State the blood parasite species.
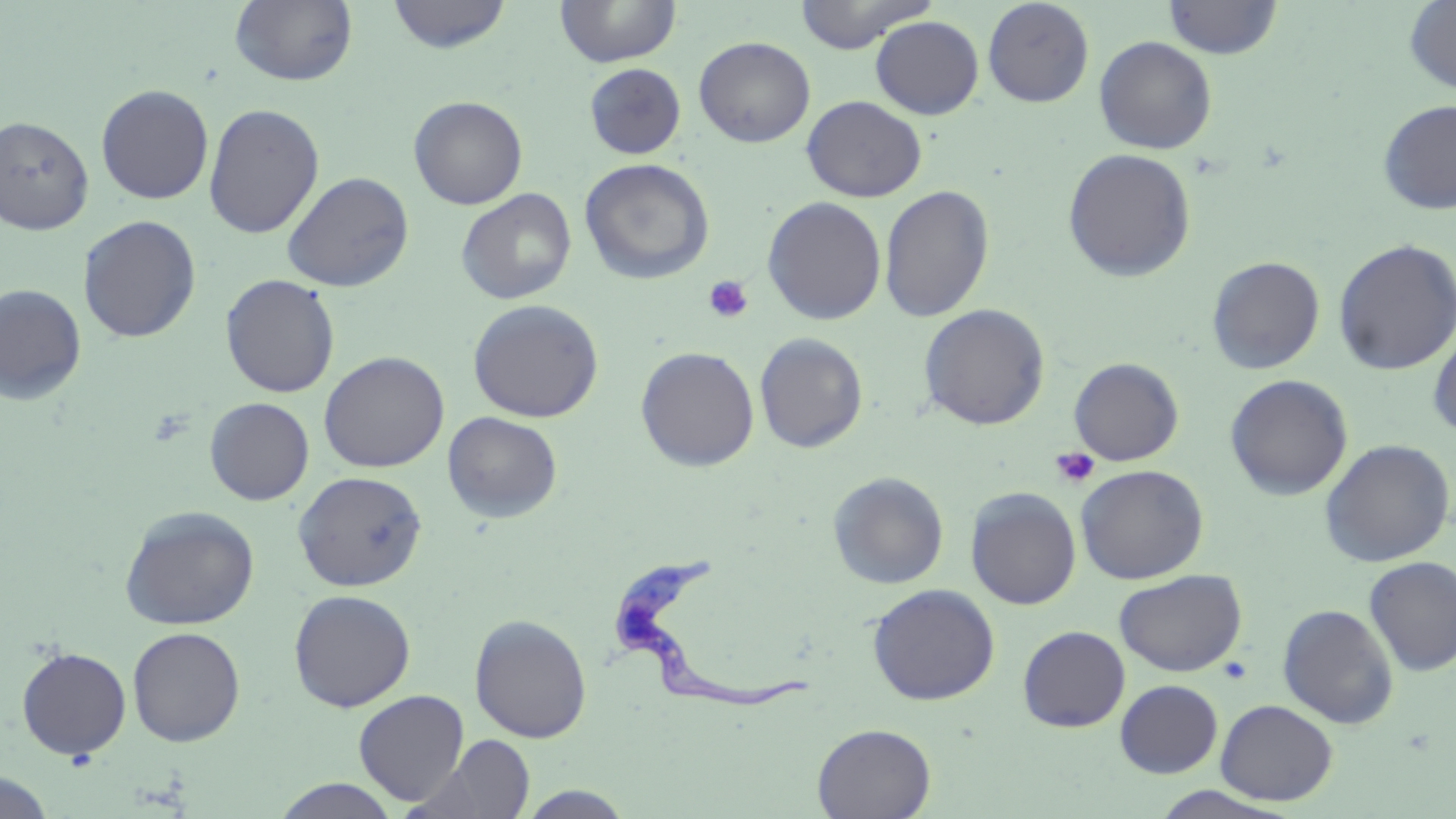

Trypanosoma brucei.

image size = 1456×819 pixels
modality = light microscopy
platelet locations = approximate bounding boxes as named x1/y1/x2/y2 corners in pixels: (x1=703, y1=275, x2=754, y2=323), (x1=1051, y1=447, x2=1100, y2=489)
uninfected red blood cell locations = approximate bounding boxes as named x1/y1/x2/y2 corners in pixels: (x1=230, y1=0, x2=358, y2=87), (x1=386, y1=0, x2=512, y2=54), (x1=555, y1=0, x2=681, y2=68), (x1=793, y1=0, x2=937, y2=53), (x1=1162, y1=0, x2=1283, y2=59), (x1=1403, y1=0, x2=1456, y2=94), (x1=982, y1=1, x2=1095, y2=107), (x1=795, y1=4, x2=979, y2=87), (x1=870, y1=15, x2=984, y2=120), (x1=1094, y1=35, x2=1217, y2=154), (x1=693, y1=36, x2=815, y2=147), (x1=583, y1=56, x2=815, y2=155), (x1=584, y1=63, x2=686, y2=160), (x1=96, y1=84, x2=214, y2=204), (x1=801, y1=95, x2=926, y2=202), (x1=409, y1=96, x2=528, y2=210), (x1=1377, y1=99, x2=1456, y2=215), (x1=204, y1=103, x2=324, y2=239), (x1=0, y1=115, x2=94, y2=235), (x1=1061, y1=148, x2=1196, y2=282), (x1=579, y1=158, x2=715, y2=285), (x1=281, y1=171, x2=414, y2=292), (x1=879, y1=184, x2=994, y2=323), (x1=455, y1=188, x2=577, y2=305), (x1=762, y1=196, x2=887, y2=325), (x1=78, y1=215, x2=201, y2=343), (x1=1333, y1=238, x2=1456, y2=376), (x1=1207, y1=256, x2=1325, y2=375), (x1=220, y1=274, x2=340, y2=398), (x1=0, y1=283, x2=87, y2=406), (x1=467, y1=298, x2=604, y2=423), (x1=918, y1=304, x2=1050, y2=430), (x1=1428, y1=326, x2=1456, y2=439), (x1=754, y1=333, x2=869, y2=453), (x1=636, y1=346, x2=760, y2=472), (x1=318, y1=351, x2=449, y2=473), (x1=1068, y1=358, x2=1184, y2=466), (x1=1225, y1=374, x2=1353, y2=501), (x1=204, y1=397, x2=314, y2=505), (x1=443, y1=412, x2=563, y2=523), (x1=1319, y1=439, x2=1455, y2=567), (x1=1075, y1=464, x2=1209, y2=584), (x1=293, y1=470, x2=427, y2=591), (x1=827, y1=471, x2=949, y2=589), (x1=965, y1=487, x2=1082, y2=610), (x1=119, y1=505, x2=260, y2=630), (x1=1363, y1=555, x2=1456, y2=676), (x1=1114, y1=569, x2=1246, y2=677), (x1=867, y1=583, x2=1000, y2=705), (x1=288, y1=589, x2=416, y2=712), (x1=1277, y1=603, x2=1399, y2=729), (x1=469, y1=614, x2=593, y2=743), (x1=1017, y1=625, x2=1130, y2=732), (x1=127, y1=626, x2=245, y2=747), (x1=16, y1=646, x2=132, y2=760), (x1=1114, y1=679, x2=1223, y2=778), (x1=353, y1=689, x2=470, y2=806), (x1=1215, y1=699, x2=1338, y2=805), (x1=812, y1=723, x2=936, y2=818), (x1=420, y1=734, x2=537, y2=819), (x1=0, y1=771, x2=56, y2=819), (x1=271, y1=778, x2=402, y2=818), (x1=515, y1=785, x2=639, y2=818), (x1=1144, y1=785, x2=1301, y2=818)
stain = May-Grünwald-Giemsa
field of view = one of a larger specimen
preparation = thin blood smear
magnification = 1000x
Trypanosoma brucei locations = approximate bounding boxes as named x1/y1/x2/y2 corners in pixels: (x1=605, y1=551, x2=817, y2=716)